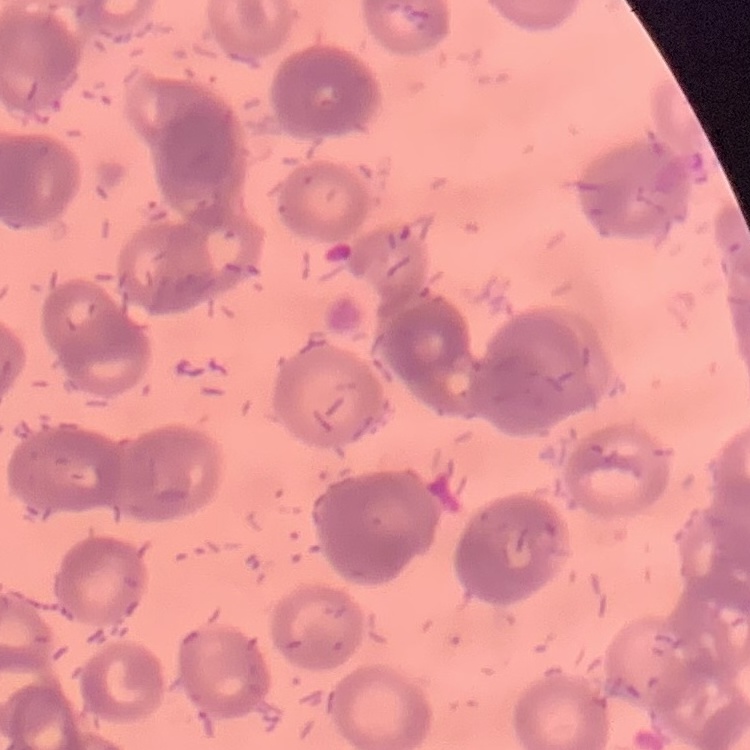

Summary:
  - Red blood cell morphology: rouleaux formation
  - Image type: one tile cut from a larger photomicrograph
  - Stain: Field's or Giemsa
  - Preparation: thin blood smear